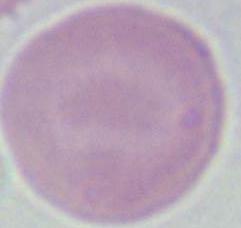 Micrograph. An erythrocyte is shown. 1000x magnification.